Locate and identify every blood parasite.
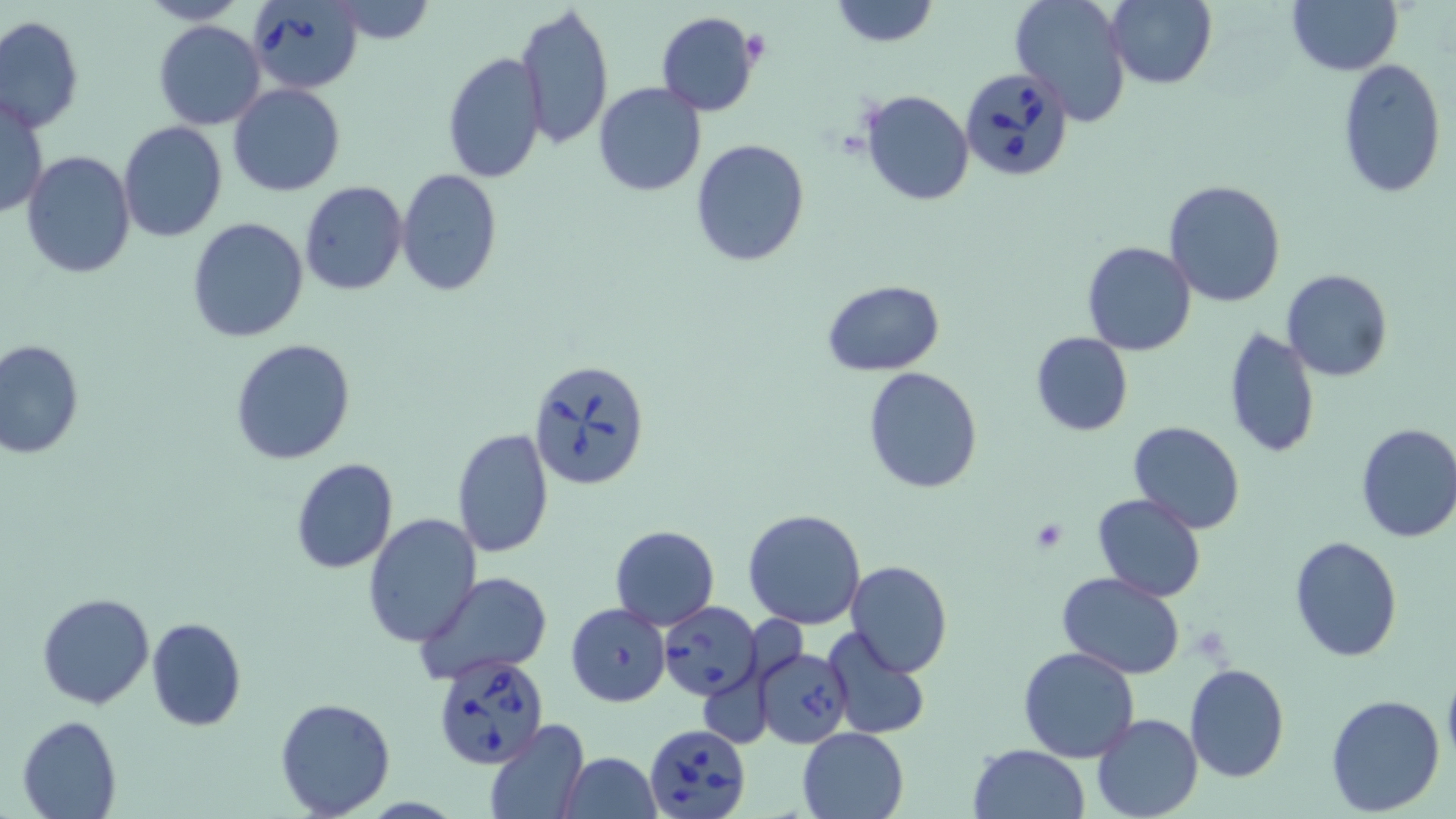
Approximate bounding boxes as named x1/y1/x2/y2 corners in pixels.
Babesia divergens-infected red blood cells: (x1=245, y1=0, x2=363, y2=94), (x1=958, y1=68, x2=1074, y2=182), (x1=529, y1=357, x2=652, y2=492), (x1=659, y1=601, x2=762, y2=700), (x1=757, y1=646, x2=853, y2=748), (x1=432, y1=652, x2=552, y2=770), (x1=646, y1=723, x2=752, y2=819).
No Plasmodium falciparum, Plasmodium ovale, Plasmodium malariae, Plasmodium vivax, or Trypanosoma brucei observed.

Summary:
  - Uninfected red blood cell locations: (x1=136, y1=0, x2=248, y2=26), (x1=828, y1=0, x2=941, y2=49), (x1=1009, y1=0, x2=1134, y2=124), (x1=1105, y1=0, x2=1217, y2=89), (x1=1286, y1=0, x2=1401, y2=75), (x1=319, y1=1, x2=441, y2=44), (x1=515, y1=2, x2=614, y2=151), (x1=656, y1=11, x2=761, y2=116), (x1=1, y1=15, x2=84, y2=133), (x1=152, y1=19, x2=267, y2=130), (x1=442, y1=52, x2=547, y2=183), (x1=1337, y1=58, x2=1447, y2=197), (x1=594, y1=83, x2=708, y2=198), (x1=228, y1=84, x2=345, y2=197), (x1=860, y1=89, x2=975, y2=206), (x1=1, y1=93, x2=48, y2=220), (x1=116, y1=122, x2=227, y2=243), (x1=690, y1=138, x2=812, y2=268), (x1=22, y1=152, x2=135, y2=278), (x1=396, y1=169, x2=503, y2=297), (x1=1164, y1=179, x2=1286, y2=307), (x1=299, y1=181, x2=408, y2=295), (x1=187, y1=217, x2=309, y2=342), (x1=1082, y1=240, x2=1197, y2=356), (x1=1282, y1=268, x2=1392, y2=383), (x1=823, y1=280, x2=944, y2=375), (x1=1223, y1=328, x2=1322, y2=461), (x1=1030, y1=332, x2=1134, y2=437), (x1=230, y1=338, x2=356, y2=466), (x1=0, y1=339, x2=84, y2=458), (x1=862, y1=367, x2=985, y2=495), (x1=1127, y1=420, x2=1248, y2=535), (x1=1353, y1=422, x2=1456, y2=544), (x1=451, y1=428, x2=553, y2=558), (x1=289, y1=457, x2=400, y2=575), (x1=1091, y1=493, x2=1208, y2=603), (x1=742, y1=508, x2=868, y2=630), (x1=362, y1=513, x2=484, y2=649), (x1=610, y1=525, x2=719, y2=629), (x1=1289, y1=535, x2=1402, y2=662), (x1=844, y1=559, x2=952, y2=677), (x1=416, y1=571, x2=552, y2=686), (x1=1056, y1=571, x2=1186, y2=676), (x1=37, y1=592, x2=156, y2=710), (x1=566, y1=603, x2=670, y2=707), (x1=146, y1=616, x2=246, y2=731), (x1=825, y1=629, x2=931, y2=738), (x1=1018, y1=646, x2=1140, y2=764), (x1=1185, y1=662, x2=1290, y2=781), (x1=1442, y1=669, x2=1456, y2=768), (x1=1324, y1=693, x2=1446, y2=816), (x1=275, y1=698, x2=396, y2=817), (x1=1091, y1=713, x2=1204, y2=819), (x1=15, y1=715, x2=121, y2=819), (x1=483, y1=720, x2=591, y2=818), (x1=797, y1=727, x2=908, y2=818), (x1=968, y1=743, x2=1089, y2=819), (x1=561, y1=751, x2=660, y2=819)
  - Slide-level diagnosis: Babesia divergens
  - Field of view: one of a larger specimen
  - Preparation: thin blood smear
  - Stain: May-Grünwald-Giemsa
  - Modality: light microscopy
  - Image size: 1456×819 pixels
  - Magnification: 1000x